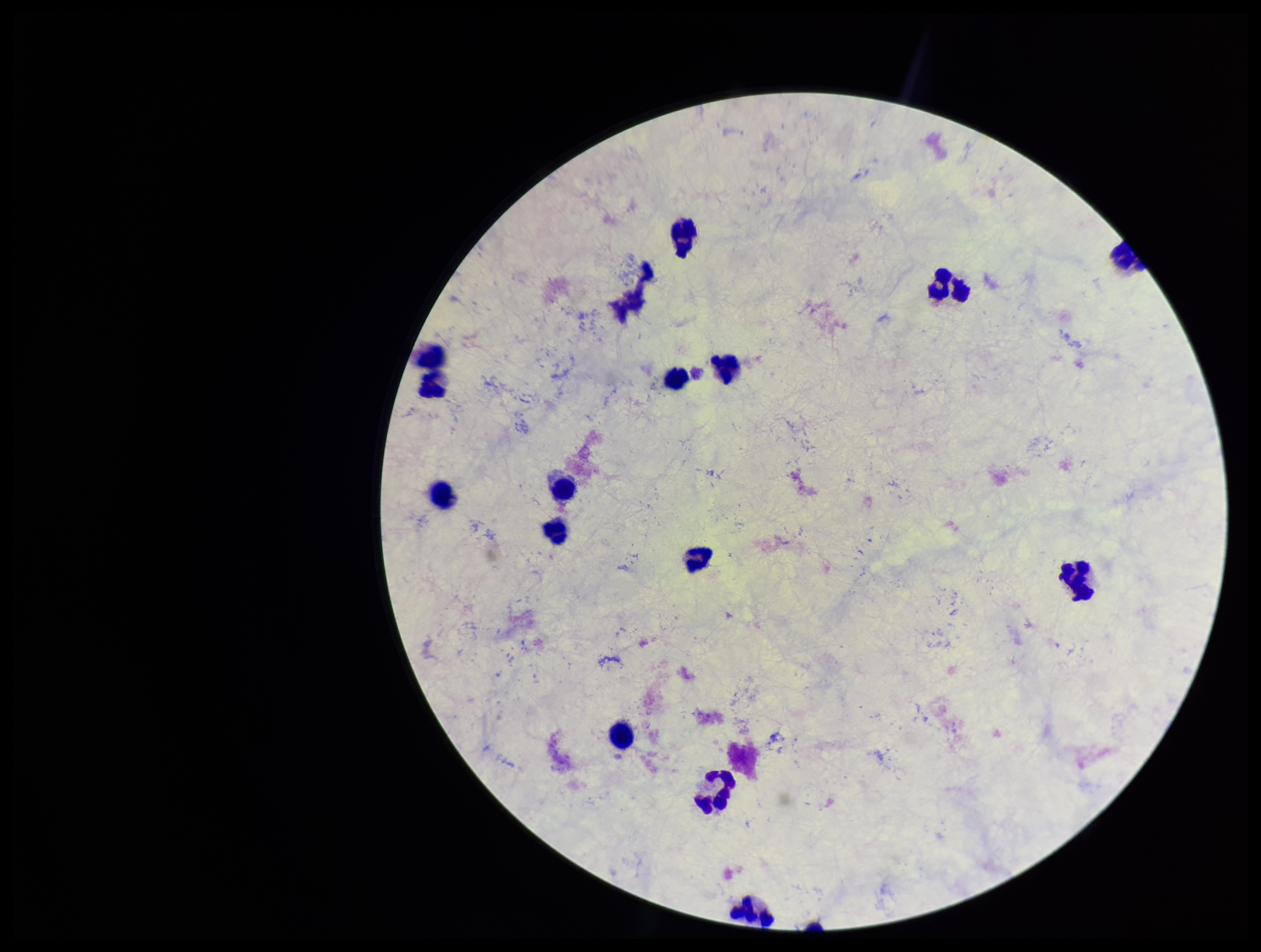

image size = 1261×952 pixels
Plasmodium parasites = none seen
parasite count = 0
leukocyte count = 17
stain = Giemsa
patient malaria status = negative
preparation = thick smear
capture = smartphone photograph through the microscope eyepiece
field of view = one from this slide